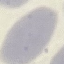 Result: negative for malaria parasites. Cell patch, automatically extracted from a larger field of view and resized to 64 × 64 pixels. Giemsa-stained preparation. Photographed with a smartphone camera at the microscope eyepiece. Thin blood film.